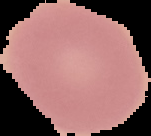

{
  "result": "negative for malaria parasites",
  "image_type": "segmented cell region with the area outside set to black",
  "preparation": "thin blood film",
  "image_size": "151×136 pixels"
}